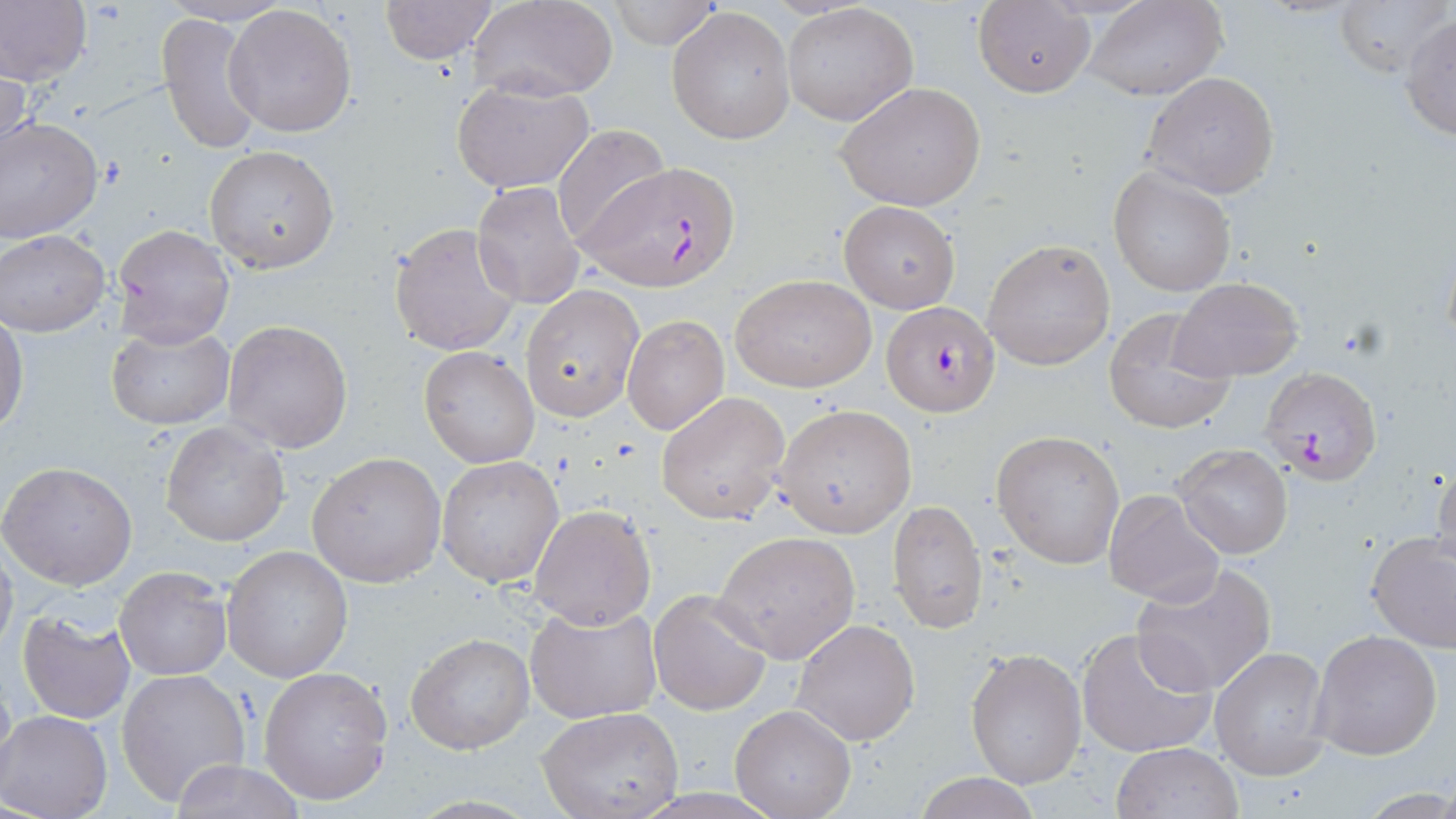

slide_level_diagnosis: Plasmodium falciparum
stain: May-Grünwald-Giemsa
field_of_view: one of a larger specimen
preparation: thin blood film
uninfected_red_blood_cell_locations: 'approximate bounding boxes as (x1, y1, x2, y2) in pixels: (0, 0, 91, 88), (380, 0, 499, 64), (606, 0, 724, 49), (1084, 0, 1227, 101), (1334, 0, 1447, 79), (466, 2, 619, 101), (782, 3, 918, 126), (974, 3, 1094, 97), (223, 4, 357, 138), (668, 6, 797, 145), (157, 12, 262, 155), (1400, 13, 1456, 141), (0, 58, 31, 172), (1141, 71, 1280, 197), (451, 77, 595, 195), (835, 81, 988, 213), (0, 117, 104, 245), (551, 123, 669, 248), (205, 145, 340, 273), (1108, 166, 1236, 297), (471, 182, 585, 311), (839, 201, 961, 313), (387, 220, 520, 357), (111, 223, 235, 347), (1, 230, 111, 337), (982, 239, 1115, 370), (730, 273, 877, 392), (1167, 276, 1304, 383), (520, 284, 644, 422), (1102, 310, 1236, 433), (0, 313, 26, 438), (623, 315, 729, 434), (222, 318, 353, 453), (106, 324, 234, 432), (419, 346, 540, 467), (656, 391, 790, 525), (774, 404, 917, 537), (160, 419, 290, 548), (992, 430, 1126, 568), (1173, 444, 1293, 560), (306, 452, 447, 587), (1431, 454, 1456, 577), (437, 456, 565, 589), (1, 460, 137, 590), (1102, 488, 1225, 607), (887, 500, 987, 634), (529, 504, 657, 629), (714, 530, 861, 664), (1366, 533, 1456, 654), (0, 540, 18, 659), (221, 545, 353, 683), (1131, 562, 1278, 697), (114, 567, 232, 681), (648, 588, 773, 716), (525, 605, 663, 723), (14, 610, 137, 725), (793, 618, 921, 747), (1077, 627, 1214, 760), (1310, 630, 1442, 760), (405, 633, 533, 755), (1209, 645, 1330, 781), (965, 648, 1086, 788), (258, 666, 395, 807), (116, 668, 251, 805), (730, 703, 857, 818), (537, 709, 684, 819), (1, 711, 114, 819), (1111, 742, 1242, 819), (171, 759, 304, 819), (910, 772, 1047, 819)'
modality: optical microscopy
plasmodium_falciparum_infected_red_blood_cell_locations: 'approximate bounding boxes as (x1, y1, x2, y2) in pixels: (583, 159, 740, 293), (880, 300, 1000, 417), (1260, 364, 1382, 485)'
image_size: 1456×819 pixels
magnification: 1000x